State which parasite is depicted.
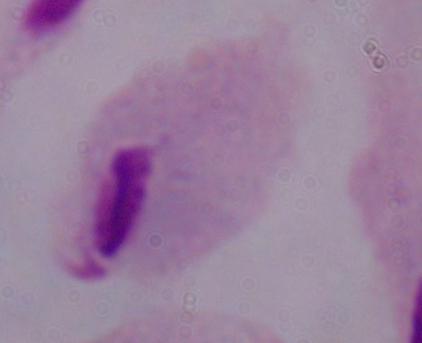

A trichomonad.

Summary:
  - Modality: photomicrograph
  - Magnification: 1000x